Outline each Trypanosoma brucei.
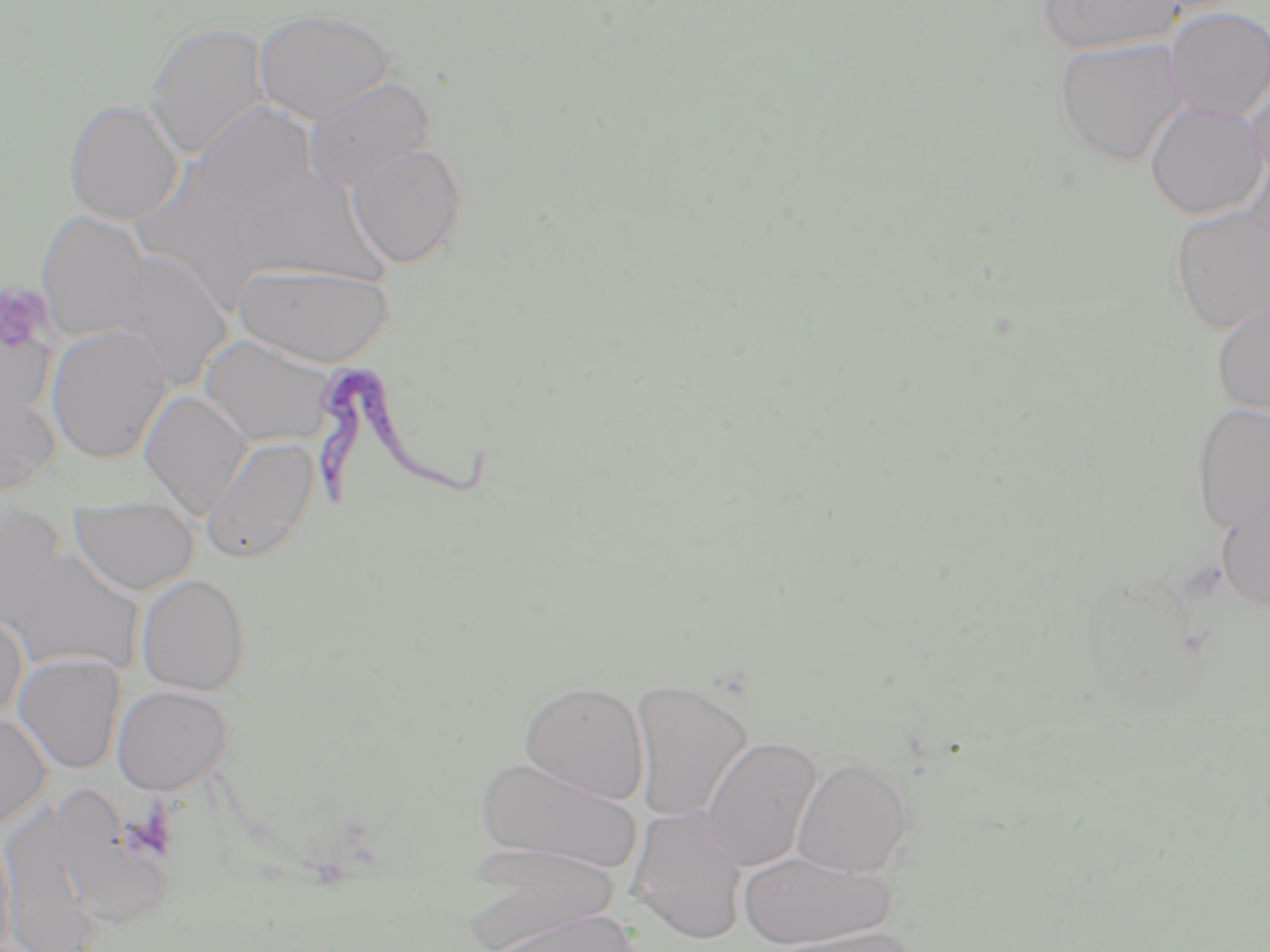

Approximate bounding boxes as (x1,y1)-(x2,y2) corner pairs in pixels.
Trypanosoma brucei: (315,358)-(497,510).

slide-level diagnosis = Trypanosoma brucei
preparation = thin blood smear
uninfected red blood cell locations = approximate bounding boxes as (x1,y1)-(x2,y2) corner pairs in pixels: (1038,0)-(1183,55), (1163,7)-(1270,122), (254,9)-(395,124), (144,22)-(270,159), (1052,37)-(1188,167), (1244,71)-(1270,187), (303,76)-(436,192), (63,98)-(184,225), (1145,100)-(1267,219), (192,101)-(317,217), (346,143)-(469,269), (1239,146)-(1270,253), (230,167)-(391,288), (1168,206)-(1270,335), (36,211)-(149,342), (111,250)-(234,394), (233,262)-(395,367), (1211,297)-(1270,417), (0,312)-(57,421), (47,325)-(170,464), (199,333)-(338,448), (0,385)-(60,497), (140,390)-(253,521), (1189,402)-(1270,534), (201,436)-(319,564), (1216,489)-(1270,609), (70,495)-(199,595), (1,505)-(67,638), (16,548)-(146,676), (136,573)-(251,695), (0,609)-(28,721), (14,654)-(125,774), (519,679)-(650,804), (629,679)-(753,824), (112,685)-(231,794), (0,713)-(51,828), (702,735)-(822,873), (475,754)-(643,876), (791,755)-(915,879), (52,784)-(182,933), (2,797)-(102,952), (627,805)-(748,944), (0,821)-(16,950), (461,842)-(620,952), (738,849)-(895,949), (477,907)-(642,952), (771,926)-(919,952)
field of view = one of a larger specimen
stain = May-Grünwald-Giemsa
magnification = 1000x
modality = optical microscopy
platelet locations = approximate bounding boxes as (x1,y1)-(x2,y2) corner pairs in pixels: (0,283)-(53,354)
image size = 1270×952 pixels